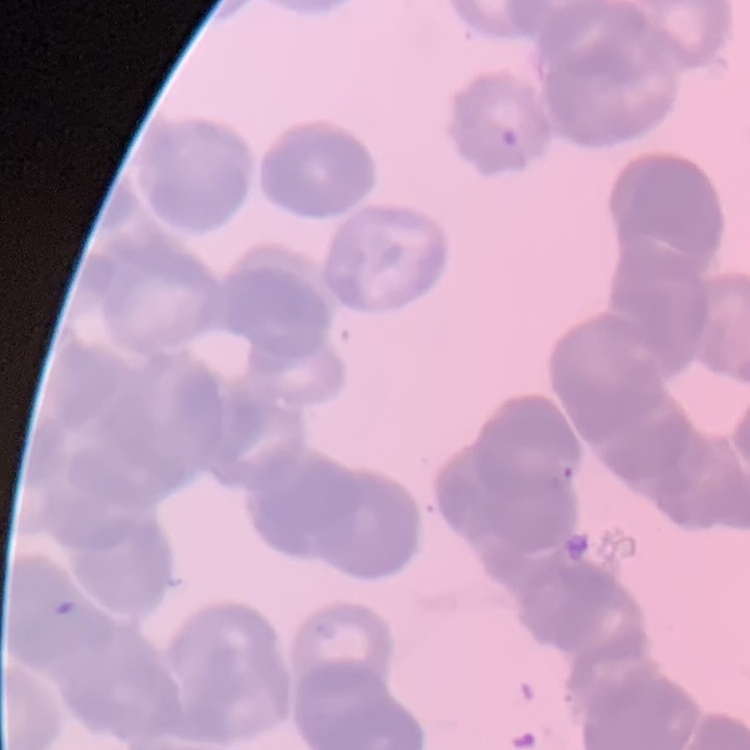
Summary:
  - Red blood cell morphology: rouleaux formation
  - Stain: Field's or Giemsa
  - Preparation: thin peripheral smear
  - Image type: square crop of a larger photomicrograph